Comment on the morphology of the erythrocytes.
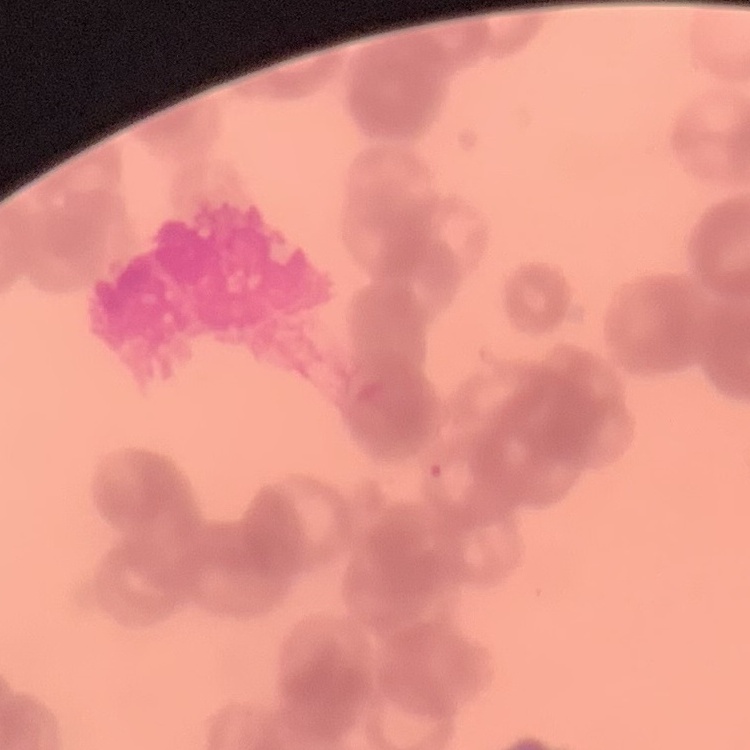

They show rouleaux formation.

preparation = thin peripheral smear
image type = square crop of a larger photomicrograph
stain = Field's or Giemsa